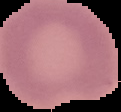
image type = segmented cell region on a black background
image size = 121×112 pixels
result = no Plasmodium parasites detected
preparation = thin blood smear